Classify this cell by malaria status.
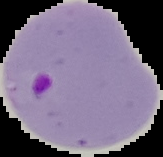
Parasitized.

Summary:
  - Image type: segmented cell region on a black background
  - Image size: 163×157 pixels
  - Preparation: thin blood film